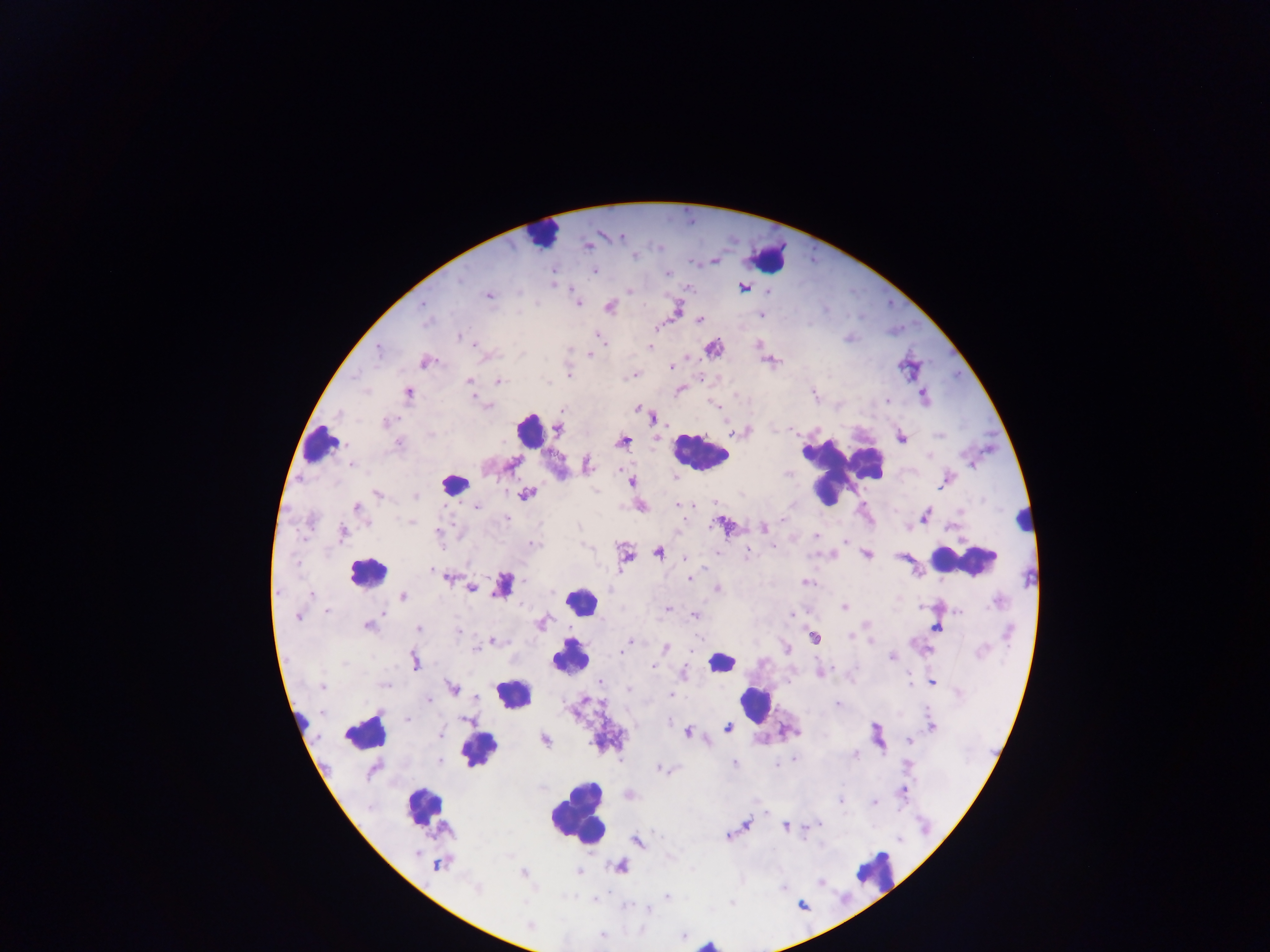

Approximate centers as [x, y] in pixels. Plasmodium parasite locations: [587, 245], [714, 260], [594, 271], [667, 273], [551, 275], [743, 287], [487, 295], [577, 304], [423, 305], [609, 306], [676, 308], [761, 314], [700, 320], [656, 325], [458, 337], [601, 338], [650, 346], [712, 347], [378, 348], [590, 353], [770, 360], [425, 361], [671, 367], [634, 374], [568, 375], [469, 381], [497, 381], [680, 389], [407, 393], [813, 394], [923, 395], [473, 396], [716, 405], [637, 408], [562, 410], [654, 416], [385, 422], [557, 428], [741, 431], [900, 437], [622, 442], [352, 463], [511, 465], [587, 465], [945, 481], [631, 482], [526, 493], [378, 494], [415, 496], [678, 504], [475, 505], [356, 507], [639, 507], [925, 516], [506, 518], [410, 521], [724, 525], [763, 527], [953, 527], [438, 533], [343, 534], [815, 535], [845, 541], [532, 544], [773, 545], [658, 552], [747, 552], [866, 553], [625, 555], [686, 558], [449, 576], [689, 577], [805, 582], [502, 584], [471, 588], [717, 589], [312, 594], [403, 596], [844, 606], [667, 608], [383, 611], [958, 611], [790, 614], [694, 616], [298, 617], [541, 622], [368, 625], [936, 627], [419, 628], [814, 636], [850, 637], [631, 640], [870, 640], [491, 641], [473, 648], [664, 648], [623, 654], [892, 656], [414, 661], [820, 670], [682, 673], [601, 682], [932, 682], [385, 684], [322, 686], [452, 688], [669, 693], [428, 699], [837, 704], [407, 718], [930, 726], [727, 728], [687, 731], [544, 739], [909, 739], [854, 754], [734, 762], [663, 769], [902, 789], [629, 794], [840, 799], [874, 802], [765, 813], [745, 824], [818, 824], [785, 826], [809, 826], [726, 835], [637, 841], [439, 864], [619, 866], [523, 874], [666, 896], [593, 900], [647, 908]. Leukocyte locations: [542, 233], [768, 257], [529, 430], [320, 444], [698, 452], [838, 467], [453, 483], [1023, 519], [963, 560], [367, 572], [581, 600], [569, 655], [721, 661], [514, 692], [755, 703], [365, 731], [479, 749], [424, 805], [576, 814], [876, 869], [707, 944]. Single field of view. Thick blood smear. Image is 1270×952 pixels. Sample from Ghana. Photographed through a microscope with a mobile-phone camera.